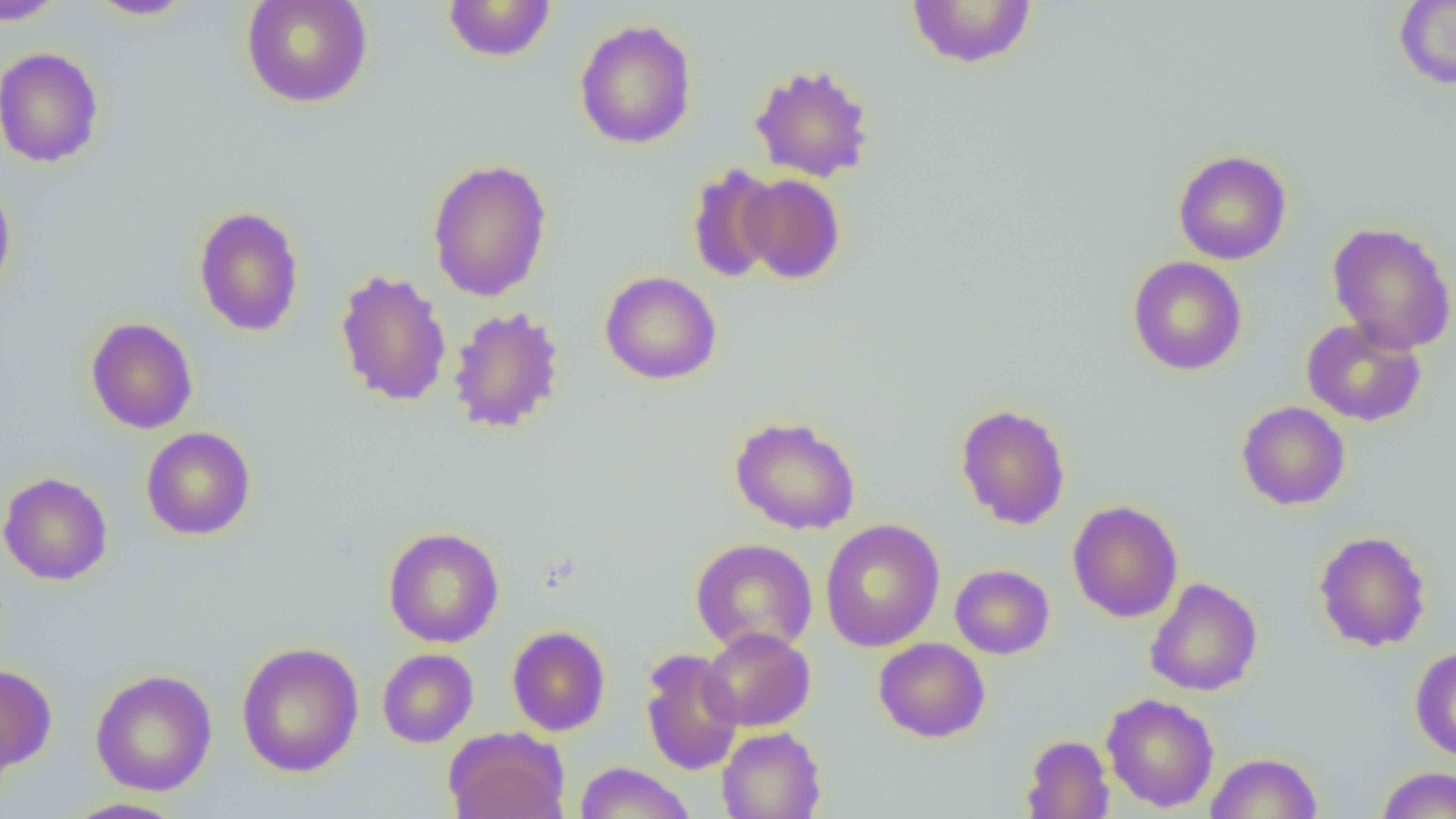

slide-level diagnosis = no evidence of blood parasites
image size = 1456×819 pixels
magnification = 1000x
field of view = one of a larger specimen
modality = optical microscopy
uninfected red blood cell locations = approximate bounding boxes as (x1,y1)-(x2,y2) corner pairs in pixels: (0,0)-(68,26), (85,0)-(195,20), (240,0)-(373,108), (905,0)-(1037,69), (1393,0)-(1456,90), (442,1)-(557,62), (575,18)-(696,149), (0,46)-(104,168), (750,63)-(875,183), (1173,150)-(1292,265), (427,158)-(552,302), (686,163)-(782,283), (0,174)-(17,302), (740,174)-(846,283), (193,205)-(305,337), (1326,221)-(1456,354), (1128,256)-(1247,376), (334,269)-(452,407), (599,270)-(722,385), (447,306)-(565,434), (85,317)-(198,434), (1301,317)-(1428,426), (1237,401)-(1350,510), (954,403)-(1071,530), (730,415)-(861,535), (140,426)-(256,540), (0,471)-(114,586), (1067,500)-(1183,623), (820,519)-(945,652), (383,526)-(504,648), (1313,530)-(1432,652), (690,538)-(818,656), (950,564)-(1055,659), (1144,577)-(1263,696), (507,625)-(611,736), (700,627)-(815,732), (873,637)-(991,743), (236,642)-(364,777), (1409,645)-(1456,762), (377,648)-(478,747), (639,648)-(744,775), (0,664)-(57,771), (90,668)-(218,796), (1102,693)-(1220,812), (716,726)-(827,819), (445,728)-(569,819), (1021,734)-(1114,818), (1205,752)-(1323,818), (574,762)-(695,819), (1376,766)-(1456,818), (63,797)-(187,819)
preparation = thin blood film